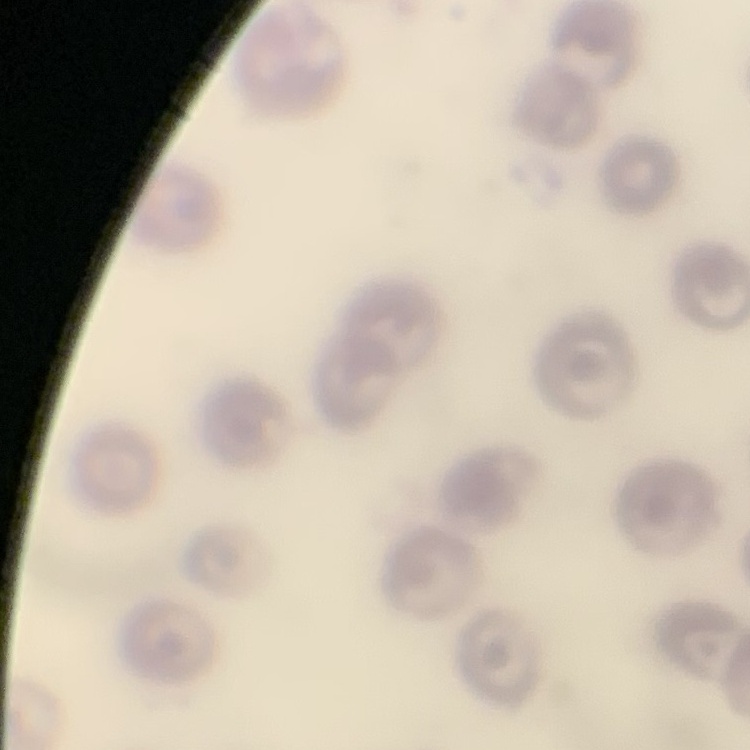

Summary:
  - Erythrocyte morphology: no rouleaux formation
  - Stain: Field's or Giemsa
  - Preparation: thin blood smear
  - Image type: square crop of a larger photomicrograph